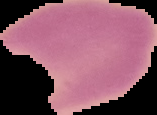
Summary:
  - Result: negative for malaria parasites
  - Preparation: thin blood smear
  - Image type: cell region segmented out of the field of view; surrounding area masked to black
  - Image size: 157×115 pixels